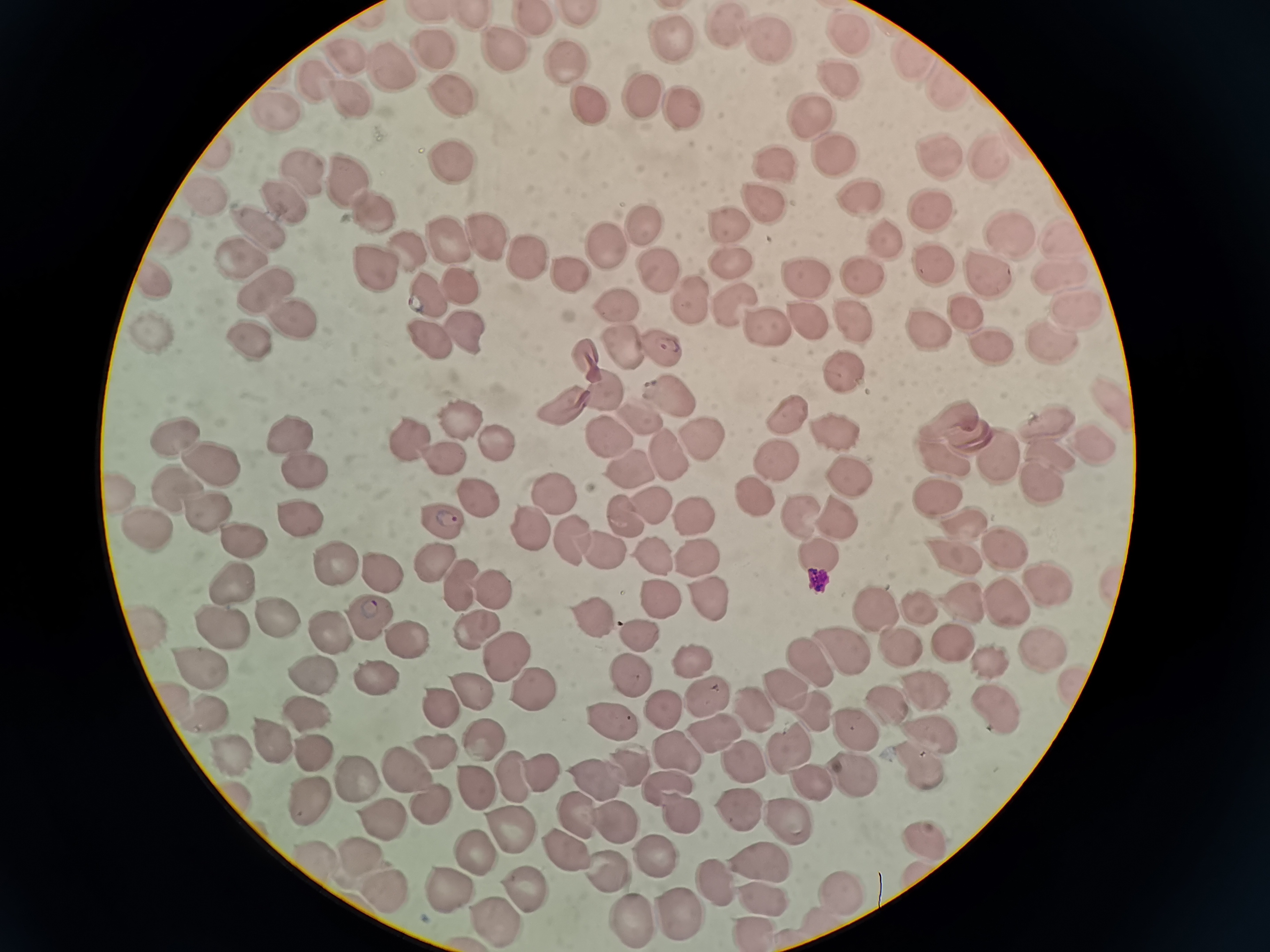

cell locations = approximate centers as (x, y) in pixels: (580, 13), (472, 17), (532, 19), (732, 28), (671, 38), (852, 38), (767, 41), (435, 52), (504, 56), (342, 57), (911, 60), (570, 63), (386, 64), (844, 78), (315, 80), (939, 81), (443, 89), (346, 96), (646, 97), (586, 107), (684, 108), (276, 109), (809, 116), (940, 155), (834, 157), (991, 159), (448, 162), (770, 166), (350, 178), (306, 179), (863, 196), (202, 197), (763, 202), (933, 208), (285, 209), (373, 213), (736, 225), (647, 227), (263, 229), (887, 235), (1006, 237), (486, 239), (175, 240), (1062, 241), (451, 246), (602, 247), (403, 249), (524, 257), (731, 259), (241, 260), (373, 264), (658, 264), (936, 268), (565, 269), (1062, 273), (985, 275), (159, 280), (857, 280), (266, 287), (806, 287), (457, 292), (696, 297), (427, 299), (615, 300), (732, 300), (967, 306), (1076, 307), (292, 316), (799, 319), (853, 321), (758, 324), (921, 324), (467, 328), (157, 330), (424, 337), (1050, 338), (253, 340), (622, 344), (658, 346), (992, 349), (584, 350), (844, 373), (598, 388), (668, 391), (1115, 401), (564, 404), (790, 412), (640, 416), (462, 419), (1052, 426), (495, 433), (605, 433), (828, 436), (294, 437), (701, 437), (179, 440), (1102, 443), (413, 449), (1051, 452), (665, 453), (770, 455), (1008, 456), (947, 457), (443, 460), (625, 460), (219, 464), (843, 467), (300, 468), (1043, 481), (181, 492), (939, 492), (757, 493), (479, 497), (126, 498), (647, 498), (551, 499), (620, 513), (801, 514), (846, 514), (215, 515), (693, 517), (447, 520), (300, 521), (523, 521), (150, 523), (963, 523), (560, 534), (248, 537), (1001, 542), (816, 547), (951, 549), (603, 550), (690, 555), (647, 557), (433, 559), (334, 566), (381, 574), (1047, 577), (458, 583), (229, 586), (493, 591), (1005, 600), (714, 601), (965, 603), (665, 605), (880, 609), (924, 609), (271, 616), (373, 621), (598, 621), (144, 626), (477, 626), (221, 627), (330, 633), (639, 633), (405, 637), (952, 641), (896, 645), (1036, 649), (503, 651), (845, 653), (986, 655), (692, 656), (813, 659), (195, 665), (311, 671), (628, 676), (380, 680), (791, 686), (536, 689), (929, 692), (471, 697), (700, 697), (173, 701), (893, 701), (661, 706), (437, 707), (991, 710), (310, 712), (755, 713), (815, 713), (211, 719), (858, 728), (614, 729), (926, 729), (714, 734), (482, 735), (271, 738), (787, 744), (431, 748), (312, 750), (675, 753), (226, 755), (918, 762), (538, 764), (744, 767), (398, 768), (853, 769), (636, 774), (351, 775), (509, 775), (468, 780), (807, 781), (664, 786), (596, 787), (305, 794), (234, 795), (677, 813), (745, 813), (579, 814), (794, 817), (614, 819), (508, 825), (922, 846), (567, 849), (316, 851), (473, 852), (360, 855), (651, 856), (760, 858), (602, 869), (713, 881), (519, 882), (442, 884), (390, 890), (837, 891), (760, 893), (676, 909), (635, 913), (496, 918), (747, 923)
preparation = thin blood film
image size = 1270×952 pixels
stain = Giemsa
capture = smartphone camera at the microscope eyepiece
field of view = single